Report the malaria status.
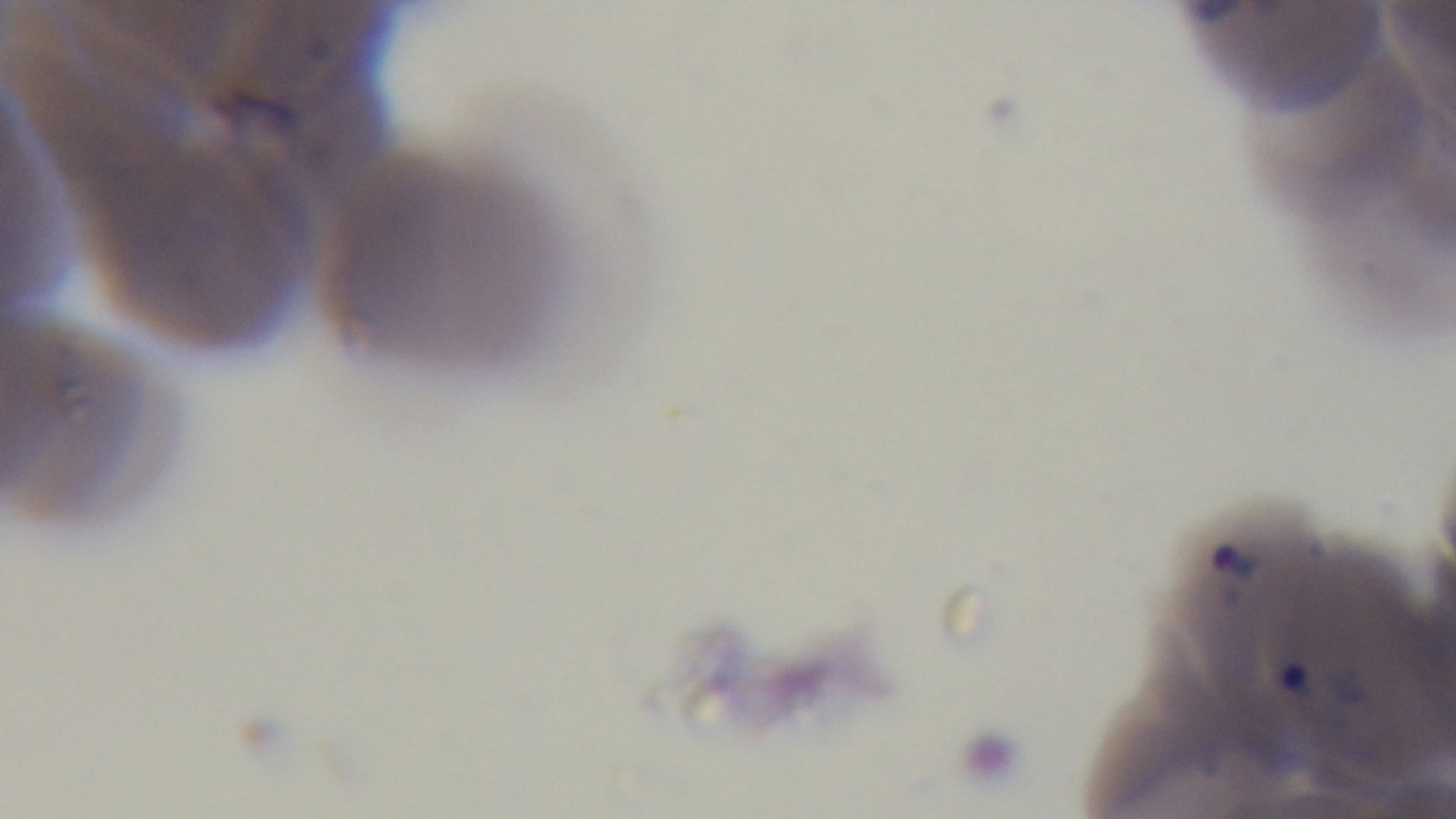

Positive.

capture = mounted 4K digital camera
preparation = thin blood film
objective = 100x oil immersion
modality = light microscopy
stain = Giemsa
field of view = single